Locate every malaria parasite by life-cycle stage, and every leukocyte.
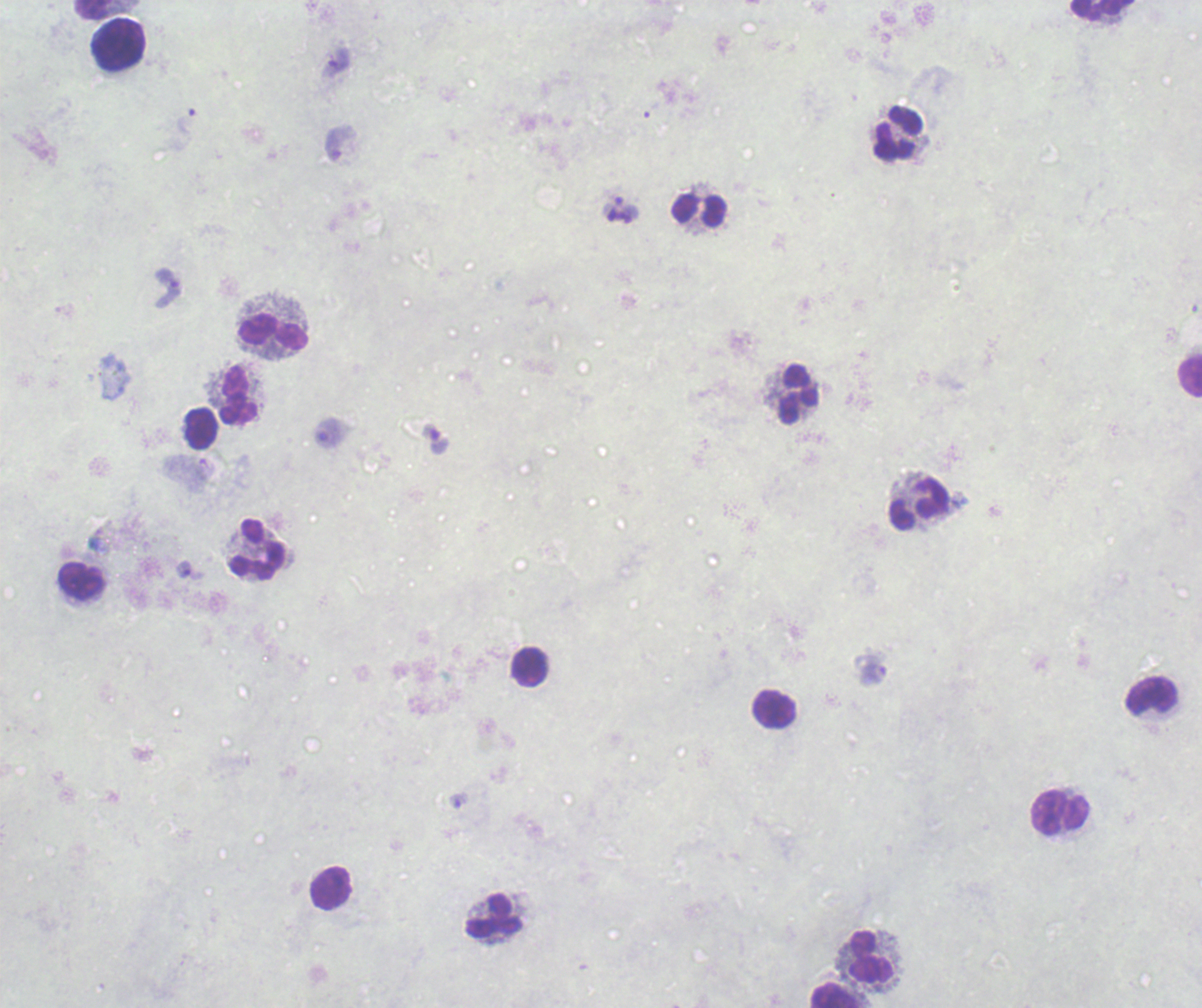
Approximate centers as (x, y) in pixels.
Trophozoites: (336, 60), (622, 209), (165, 288), (433, 439), (191, 571), (870, 670), (459, 801).
No schizont or gametocyte forms observed.
Leukocytes: (93, 9), (1100, 9), (118, 43), (898, 133), (699, 210), (272, 333), (1189, 377), (237, 395), (798, 395), (200, 428), (918, 504), (256, 549), (81, 581), (529, 667), (1151, 696), (773, 709), (1060, 812), (331, 887), (494, 915), (871, 956), (835, 995).

{
  "magnification": "100x",
  "context": "previously used in an actual diagnosis",
  "background_quality": "poor",
  "stain": "Romanowsky",
  "field_of_view": "one from this slide",
  "image_size": "1202×1008 pixels",
  "preparation": "thick blood film"
}